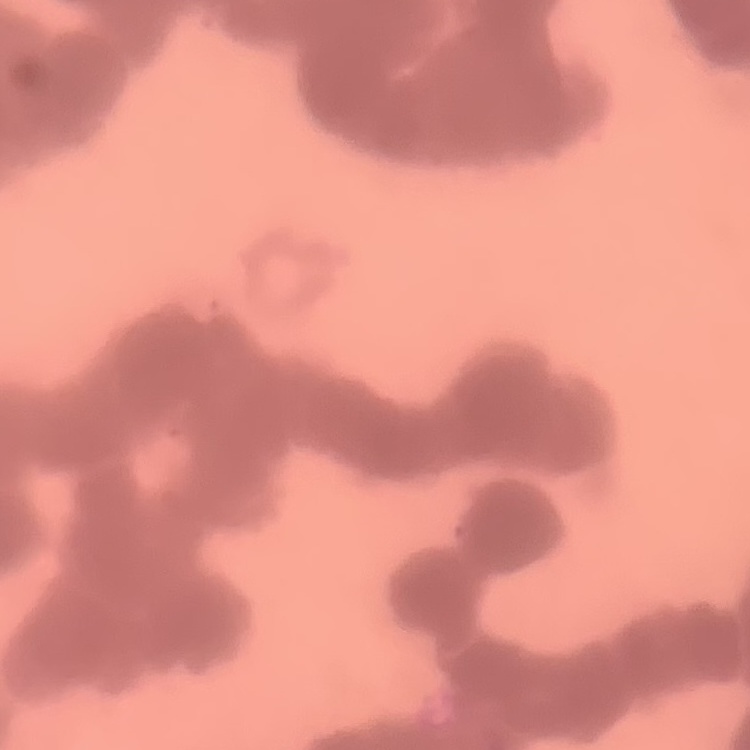

erythrocyte_morphology: rouleaux formation
image_type: one tile cut from a larger photomicrograph
preparation: thin blood smear
stain: Field's or Giemsa